Assess this cell for malaria.
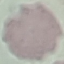
Uninfected.

Summary:
  - Stain: Giemsa
  - Capture: smartphone camera at the microscope eyepiece
  - Preparation: thin smear
  - Image type: automatically extracted cell patch, resized to 64 × 64 pixels